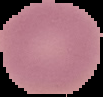

From a thin blood smear. Image is 103×97 pixels. Cell region segmented out of the field of view; the surrounding area is masked to black. Result: negative for Plasmodium parasites.